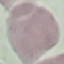

malaria_status: uninfected
capture: smartphone camera at the microscope eyepiece
image_type: cell patch, automatically extracted from a larger field of view and resized to 64 × 64 pixels
preparation: thin smear
stain: Giemsa